Describe the morphology of the red blood cells.
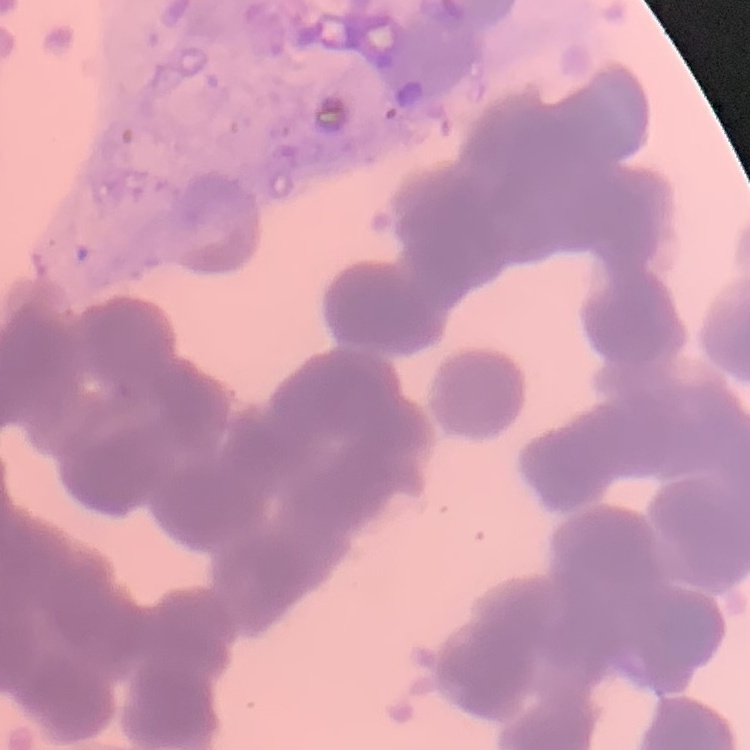

They show rouleaux formation.

Summary:
  - Preparation: thin peripheral smear
  - Image type: square crop of a larger photomicrograph
  - Stain: Field's or Giemsa